Describe the morphology of the red blood cells.
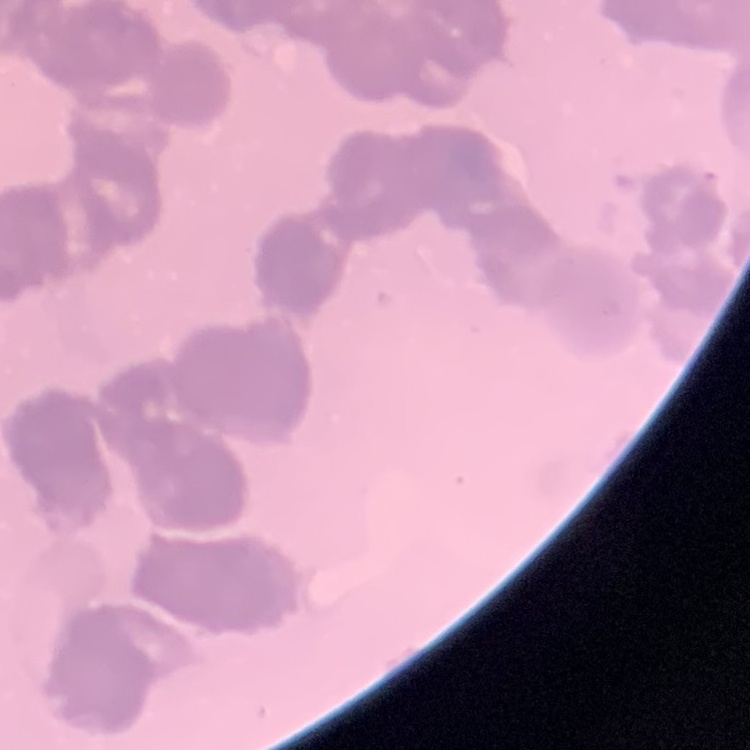
They show rouleaux formation.

Square crop of a larger photomicrograph. Stained with either Field's or Giemsa. Thin blood smear.